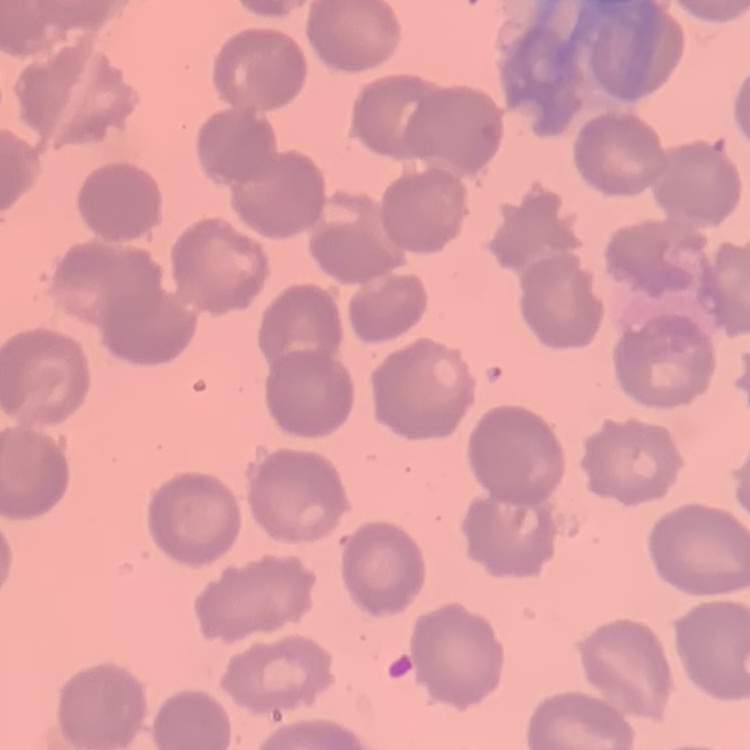
The erythrocytes exhibit no rouleaux formation. Thin blood film. Stained with either Field's or Giemsa. Square crop of a larger photomicrograph.